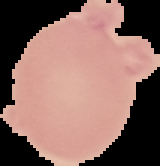

result = negative for malaria parasites
image size = 160×166 pixels
preparation = thin blood smear
image type = cell region segmented out of the field of view; surrounding area masked to black